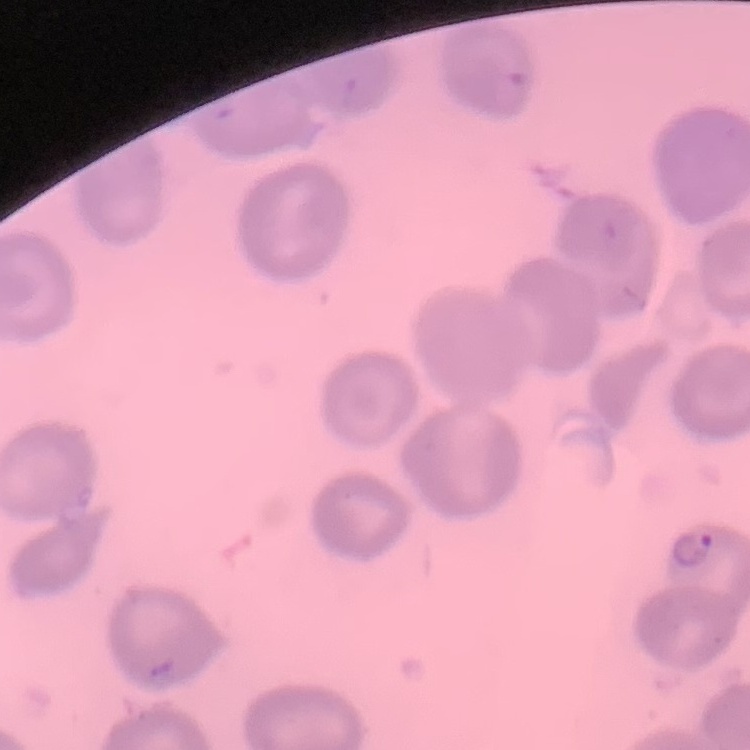
Summary:
  - Erythrocyte morphology: no rouleaux formation
  - Image type: square crop of a larger photomicrograph
  - Preparation: thin peripheral smear
  - Stain: Field's or Giemsa